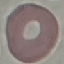 Malaria status: uninfected. Thin smear of blood. Cell patch, automatically extracted from a larger field of view and resized to 64 × 64 pixels. Giemsa stain. Acquired by smartphone through the microscope eyepiece.